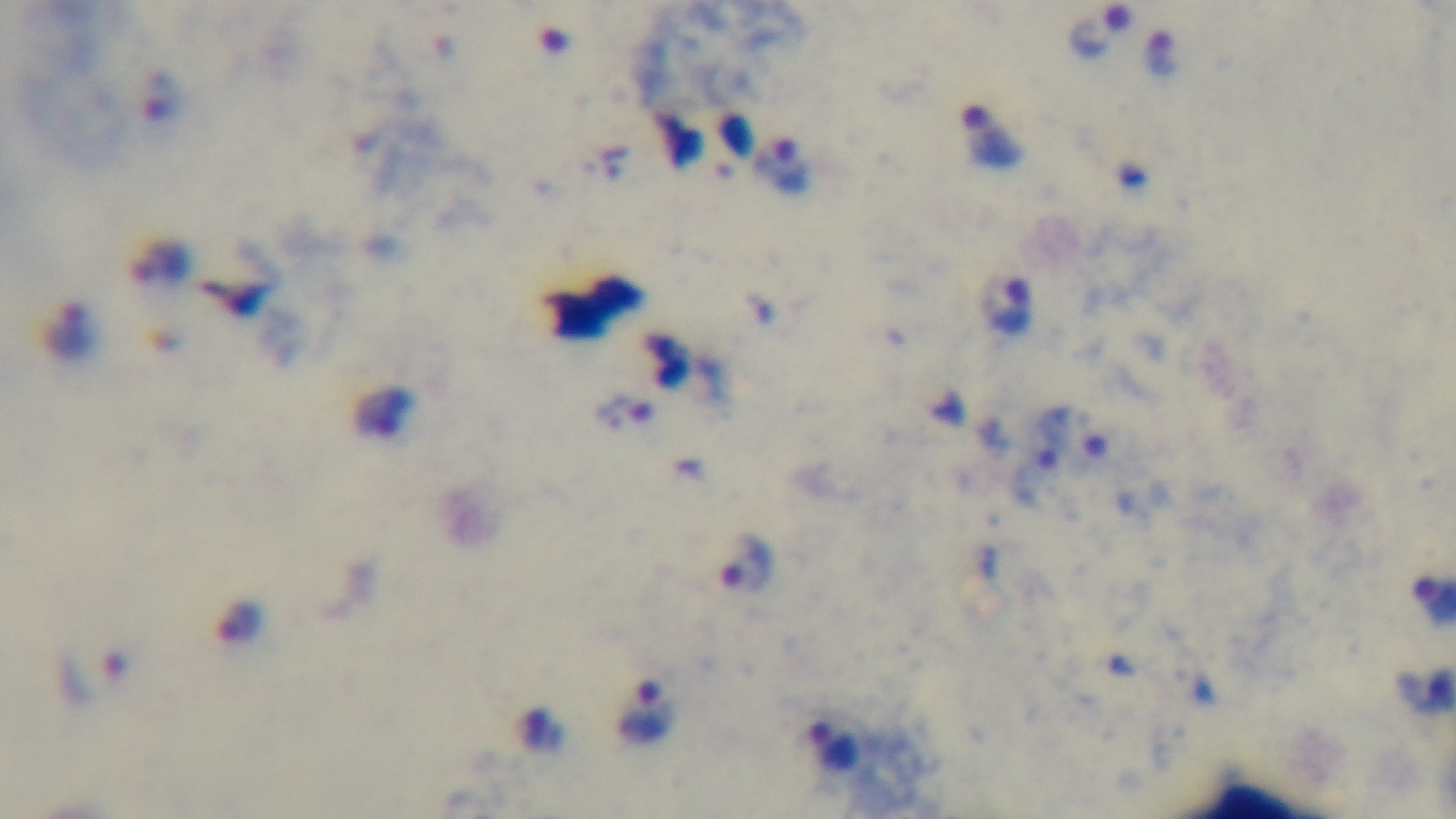

Summary:
  - Capture: mounted 4K digital camera
  - Objective: 100x oil immersion
  - Malaria status: infected
  - Stain: Giemsa
  - Preparation: thick
  - Modality: light microscopy
  - Field of view: one from the slide